Classify this cell by malaria status.
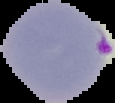
It is parasitized.

image_type: cell region segmented out of the field of view; surrounding area masked to black
image_size: 115×103 pixels
preparation: thin blood smear